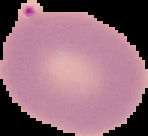

Segmented cell region on a black background. Malaria status: uninfected. Image is 148×136 pixels. From a thin blood smear.